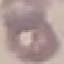
Result: no malaria parasites seen. Giemsa-stained preparation. Cell patch, automatically extracted from a larger field of view and resized to 64 × 64 pixels. Photographed with a smartphone camera at the microscope eyepiece. Thin blood smear.